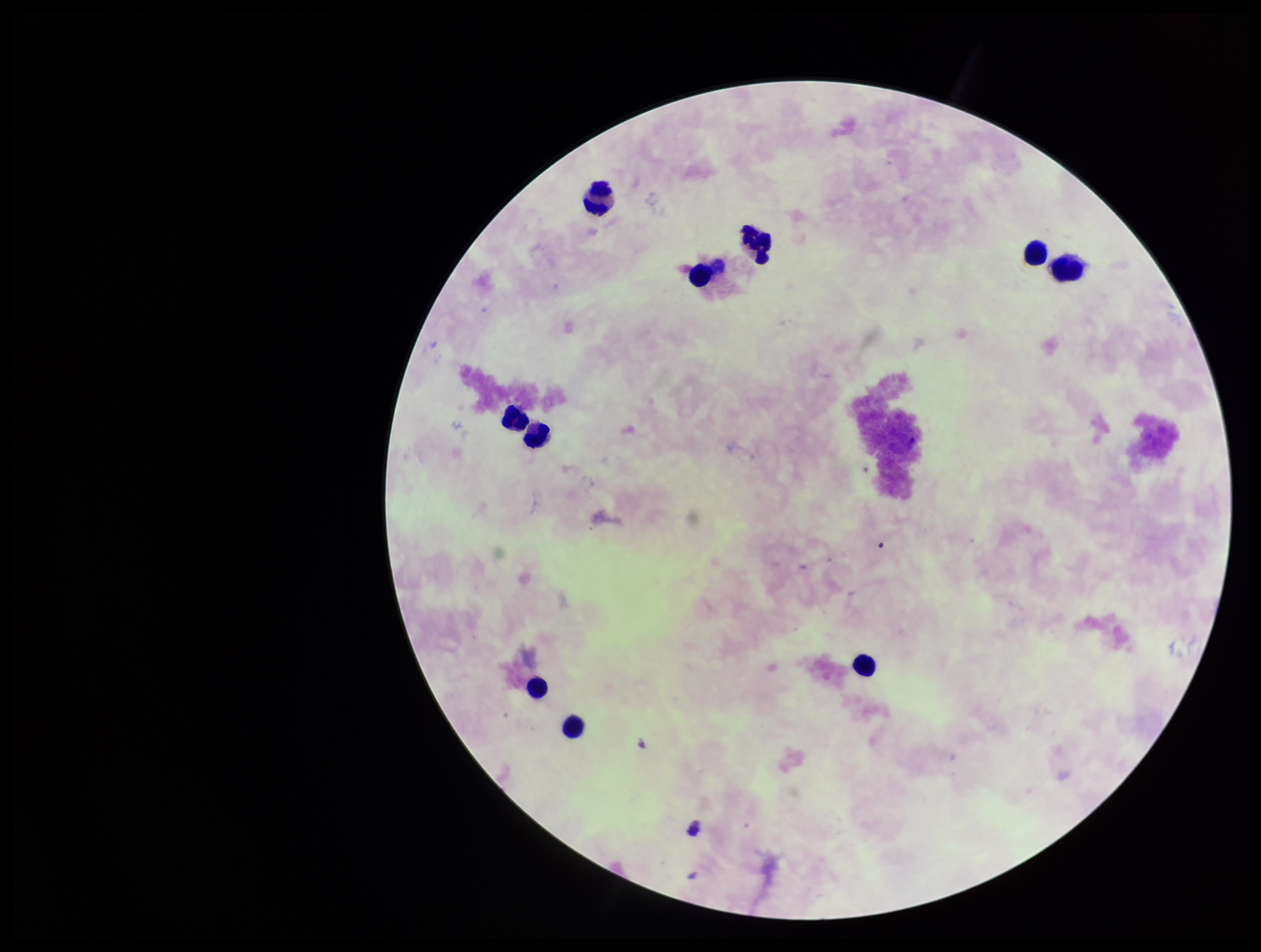 Preparation: thick blood smear. Parasite count: 0. Smartphone photograph taken through the eyepiece of a microscope. Single field of view. Leukocyte count: 10. Plasmodium parasites: none seen. Patient malaria status: negative. Giemsa stain. Image is 1261×952 pixels.